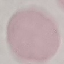
Malaria status: uninfected. Photographed with a smartphone camera at the microscope eyepiece. Thin blood smear. Giemsa stain. Automatically extracted cell patch, resized to 64 × 64 pixels.